Classify this cell by malaria status.
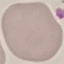

It is uninfected.

image type = cell patch, automatically extracted from a larger field of view and resized to 64 × 64 pixels
stain = Giemsa
capture = smartphone through the microscope eyepiece
preparation = thin smear